Report the malaria status of this cell.
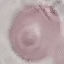
Uninfected.

Giemsa-stained preparation. Cell patch, automatically extracted from a larger field of view and resized to 64 × 64 pixels. Photographed with a smartphone camera at the microscope eyepiece. Thin blood film.